Assess this cell for malaria.
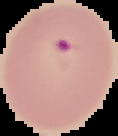

It is parasitized.

Summary:
  - Image size: 118×136 pixels
  - Preparation: thin blood film
  - Image type: segmented cell region with the area outside set to black